Assess this cell for malaria.
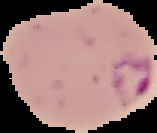
Parasitized.

Summary:
  - Image size: 157×133 pixels
  - Image type: segmented cell region with the area outside set to black
  - Preparation: thin blood film